Assess the morphology of the erythrocytes.
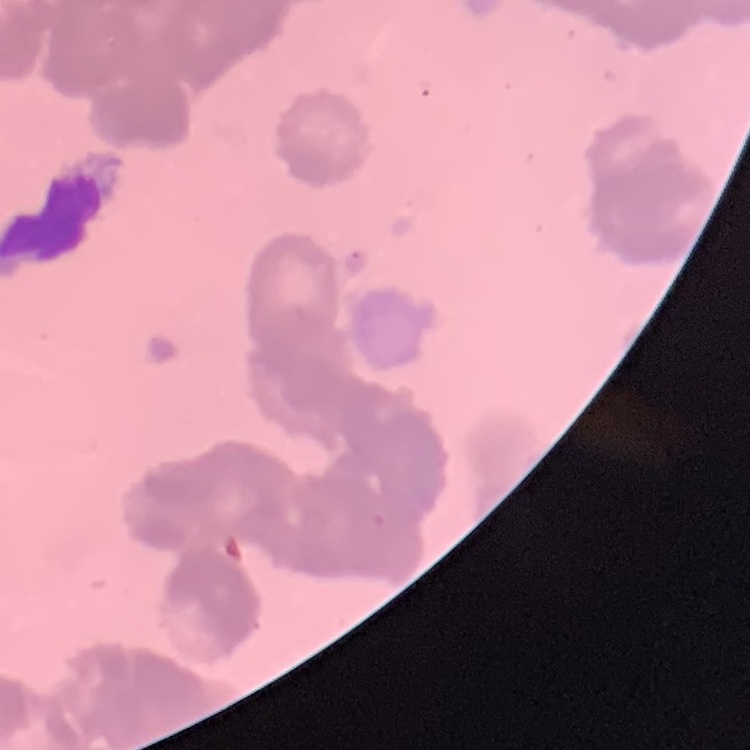
They show rouleaux formation.

One tile cut from a larger photomicrograph. Thin peripheral smear. Stained with either Field's or Giemsa.